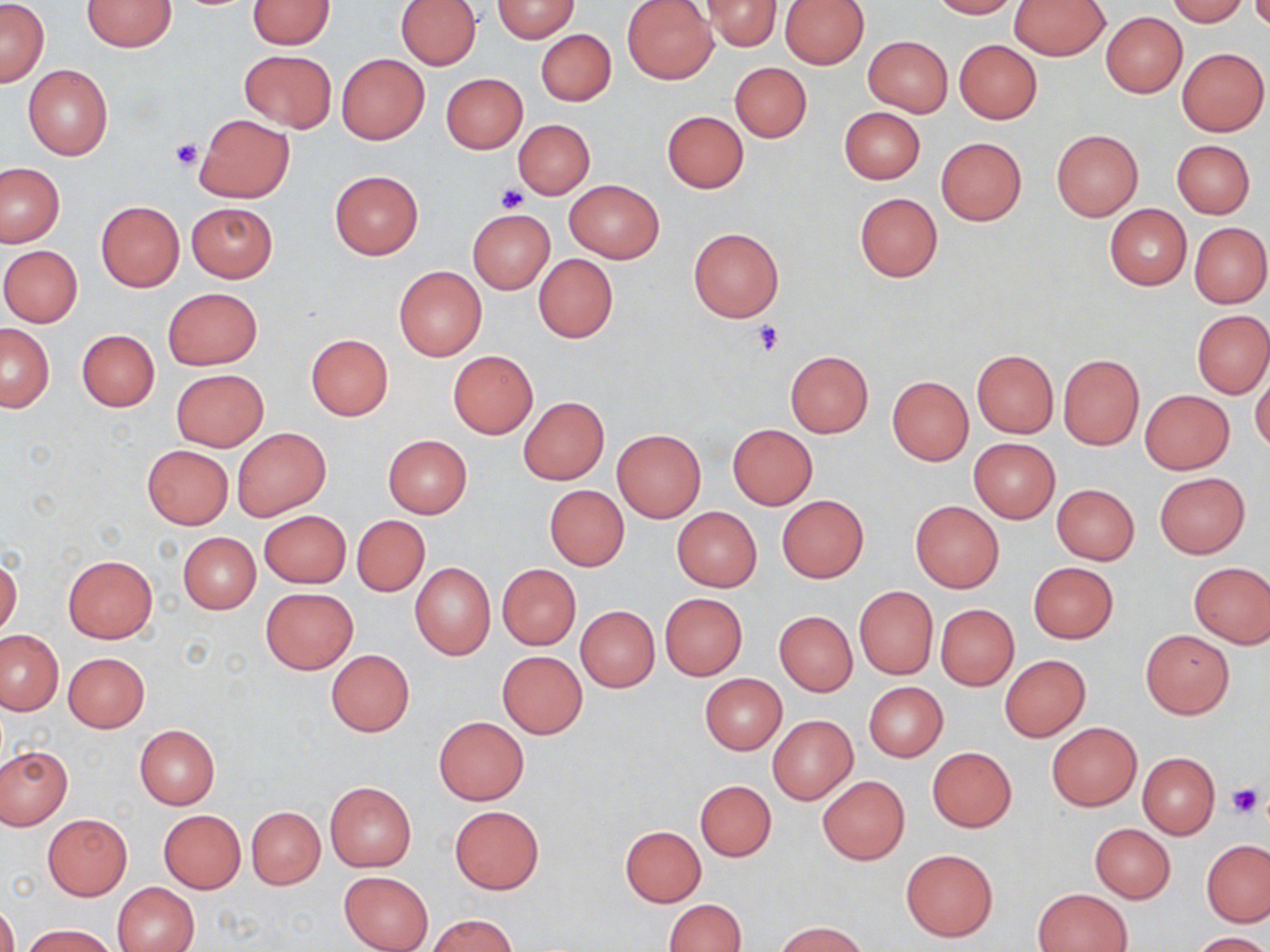

Approximate bounding boxes as (x1, y1, x2, y2) in pixels. Uninfected red blood cell locations: (82, 0, 175, 51), (246, 0, 335, 48), (395, 0, 481, 69), (703, 0, 781, 51), (928, 0, 1020, 18), (1166, 0, 1251, 26), (0, 1, 48, 87), (492, 1, 579, 42), (622, 1, 718, 84), (780, 1, 868, 69), (1010, 1, 1110, 60), (1100, 12, 1187, 97), (536, 29, 615, 106), (864, 36, 952, 116), (954, 39, 1042, 123), (1177, 48, 1268, 136), (238, 50, 336, 133), (337, 53, 429, 145), (730, 61, 812, 142), (23, 65, 112, 160), (440, 73, 528, 153), (839, 107, 925, 184), (661, 111, 748, 193), (194, 114, 294, 202), (513, 119, 595, 198), (1051, 129, 1142, 220), (936, 137, 1026, 225), (1171, 139, 1255, 218), (0, 163, 64, 247), (329, 170, 424, 260), (565, 180, 664, 262), (855, 193, 942, 281), (95, 202, 184, 292), (186, 202, 278, 282), (1105, 204, 1190, 290), (467, 209, 555, 294), (1189, 222, 1270, 308), (688, 228, 783, 321), (0, 245, 82, 326), (534, 254, 618, 342), (393, 266, 487, 361), (163, 288, 262, 369), (1192, 309, 1270, 398), (1, 323, 54, 412), (76, 329, 160, 411), (305, 334, 394, 421), (972, 350, 1059, 437), (448, 351, 538, 438), (785, 351, 873, 437), (1057, 353, 1144, 450), (1251, 368, 1270, 455), (171, 369, 268, 450), (887, 375, 974, 465), (1140, 390, 1235, 474), (519, 397, 609, 485), (728, 424, 817, 509), (232, 427, 331, 521), (612, 429, 707, 523), (383, 435, 472, 517), (968, 437, 1060, 523), (142, 445, 233, 529), (1154, 472, 1250, 558), (1052, 483, 1139, 564), (544, 485, 629, 571), (777, 496, 868, 581), (909, 499, 1004, 593), (671, 507, 762, 591), (259, 510, 350, 587), (352, 515, 429, 596), (179, 533, 260, 613), (63, 555, 158, 643), (0, 558, 22, 638), (409, 562, 495, 659), (1028, 562, 1119, 643), (1188, 562, 1270, 647), (497, 565, 581, 650), (854, 587, 938, 679), (260, 588, 358, 674), (659, 593, 746, 681), (936, 604, 1019, 690), (576, 606, 660, 692), (774, 611, 857, 696), (0, 629, 65, 715), (1140, 630, 1234, 718), (326, 649, 415, 737), (498, 651, 586, 737), (63, 653, 148, 732), (1000, 655, 1090, 740), (700, 673, 787, 754), (863, 682, 948, 761), (768, 716, 858, 804), (434, 717, 527, 804), (1047, 722, 1141, 810), (134, 724, 220, 808), (0, 746, 72, 828), (927, 747, 1017, 832), (1138, 752, 1219, 838), (817, 776, 909, 865), (695, 781, 776, 861), (325, 782, 416, 871), (449, 806, 544, 894), (247, 807, 324, 889), (158, 810, 245, 893), (43, 814, 131, 899), (1089, 823, 1175, 902), (620, 826, 706, 906), (1201, 839, 1269, 927), (900, 849, 998, 941), (339, 871, 434, 952), (112, 881, 199, 952), (1033, 890, 1130, 951), (663, 899, 746, 952), (0, 900, 18, 952), (430, 915, 517, 952), (775, 921, 867, 952), (24, 923, 118, 952), (1191, 932, 1268, 952). Platelet locations: (171, 139, 202, 170), (496, 185, 527, 213), (754, 320, 786, 355), (1225, 782, 1265, 820). Slide-level diagnosis: no evidence of blood parasites. Captured at 1000x magnification. Single field of view. Thin blood film. May-Grünwald-Giemsa stain. Image is 1270×952 pixels. Optical microscopy.